Name the parasite shown.
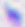

This is Toxoplasma gondii.

Summary:
  - Magnification: 400x
  - Modality: photomicrograph